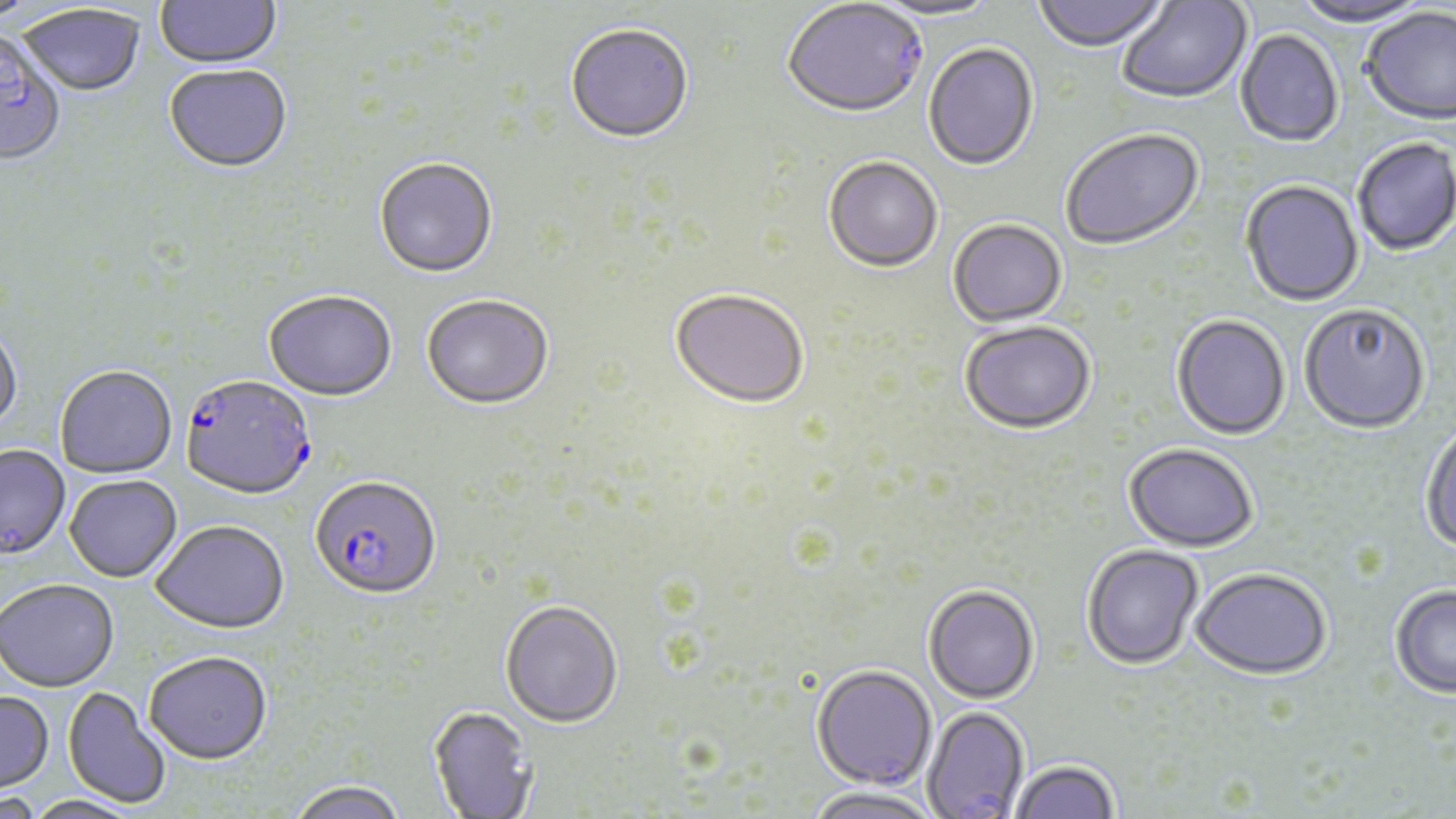
Approximate bounding boxes as (x1,y1)-(x2,y2) corner pairs in pixels. Uninfected red blood cell locations: (1031,0)-(1171,55), (1290,0)-(1434,29), (155,1)-(282,71), (866,1)-(1002,23), (1117,1)-(1252,105), (17,5)-(146,98), (1361,9)-(1456,128), (565,25)-(694,146), (0,31)-(66,168), (1235,31)-(1344,149), (923,44)-(1040,173), (163,65)-(293,175), (1061,130)-(1205,252), (1353,139)-(1456,257), (823,158)-(942,274), (374,159)-(498,280), (1240,181)-(1364,308), (948,220)-(1067,329), (670,290)-(810,409), (263,291)-(398,403), (421,296)-(553,411), (1299,305)-(1431,435), (1171,316)-(1291,440), (959,320)-(1096,434), (0,323)-(22,435), (54,366)-(177,479), (1420,421)-(1456,554), (1124,442)-(1259,551), (0,445)-(71,561), (64,476)-(182,583), (150,520)-(289,635), (1081,543)-(1204,669), (1190,566)-(1332,677), (0,580)-(119,694), (923,583)-(1040,703), (1390,584)-(1456,698), (500,599)-(623,727), (144,652)-(272,766), (811,664)-(936,790), (62,688)-(172,809), (0,692)-(54,795), (427,705)-(536,818), (922,705)-(1029,817), (1009,759)-(1119,819), (286,780)-(407,819), (803,787)-(942,819), (0,793)-(43,819), (20,796)-(144,819). Plasmodium falciparum-infected red blood cell locations: (782,2)-(928,121), (180,376)-(316,501), (310,476)-(442,601). Slide-level diagnosis: Plasmodium falciparum. 1000x magnification. Thin blood film. Image is 1456×819 pixels. May-Grünwald-Giemsa stain. Light microscopy. One field of a larger specimen.